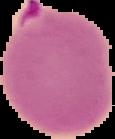

Result: Plasmodium parasites identified. From a thin blood smear. Segmented cell region on a black background. Image is 115×139 pixels.